Locate and identify every blood parasite.
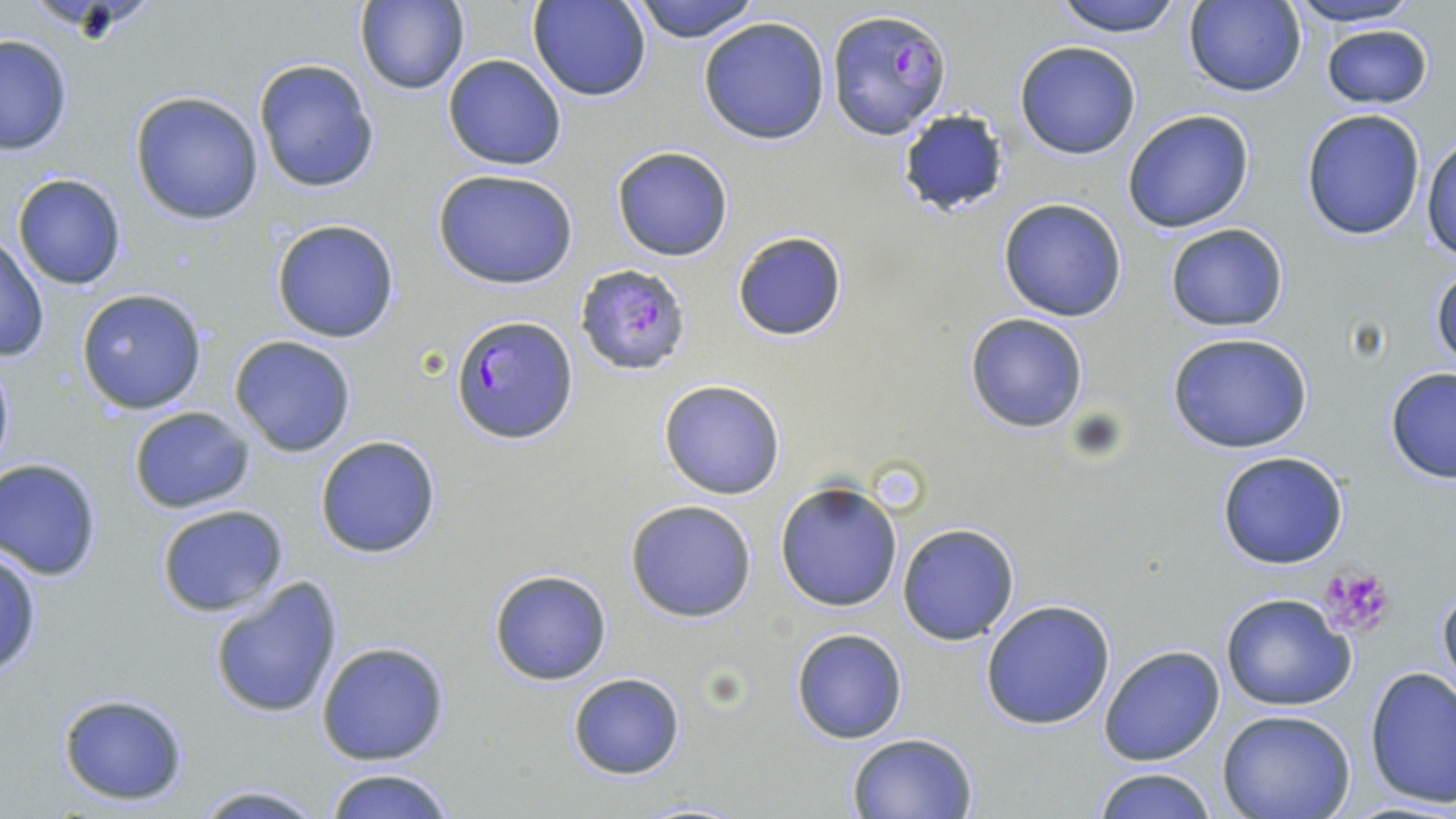

Approximate bounding boxes as [x1, y1, x2, y2] in pixels.
Plasmodium falciparum-infected red blood cells: [826, 7, 950, 139], [575, 262, 692, 376], [450, 313, 578, 445].
No Plasmodium ovale, Plasmodium malariae, Plasmodium vivax, Babesia divergens, or Trypanosoma brucei observed.

Uninfected red blood cell locations: [632, 0, 762, 44], [1047, 0, 1189, 37], [1279, 0, 1428, 28], [354, 1, 470, 96], [530, 1, 652, 102], [1182, 1, 1307, 97], [699, 15, 831, 145], [1321, 23, 1435, 110], [0, 34, 73, 156], [1014, 40, 1142, 159], [442, 54, 566, 171], [253, 57, 380, 194], [129, 90, 264, 225], [896, 108, 1011, 214], [1121, 108, 1256, 234], [1300, 109, 1427, 240], [1421, 132, 1456, 262], [611, 145, 735, 261], [431, 167, 579, 289], [12, 172, 127, 290], [999, 198, 1128, 321], [270, 218, 400, 342], [1165, 223, 1290, 332], [732, 230, 846, 342], [0, 236, 50, 364], [1428, 261, 1456, 375], [75, 288, 208, 415], [964, 312, 1089, 432], [1166, 331, 1313, 453], [229, 335, 357, 457], [0, 352, 16, 485], [1384, 366, 1456, 485], [658, 379, 786, 500], [128, 406, 257, 513], [315, 434, 442, 559], [1215, 450, 1350, 569], [0, 457, 103, 580], [774, 478, 904, 614], [625, 498, 760, 623], [154, 504, 292, 618], [897, 524, 1019, 645], [0, 543, 42, 679], [487, 569, 613, 686], [208, 577, 345, 720], [1436, 578, 1456, 698], [1221, 593, 1355, 711], [979, 600, 1116, 730], [790, 628, 908, 744], [315, 639, 450, 766], [1098, 643, 1226, 767], [1364, 665, 1456, 810], [567, 672, 686, 779], [57, 691, 191, 807], [1218, 712, 1355, 819], [846, 731, 979, 819], [321, 766, 457, 819], [1089, 766, 1221, 819], [185, 783, 331, 818], [625, 798, 751, 817]. Platelet locations: [1317, 566, 1396, 638]. Slide-level diagnosis: Plasmodium falciparum. Image is 1456×819 pixels. May-Grünwald-Giemsa-stained preparation. 1000x magnification. Thin blood film. Single field of view. Light microscopy.